State the blood parasite species.
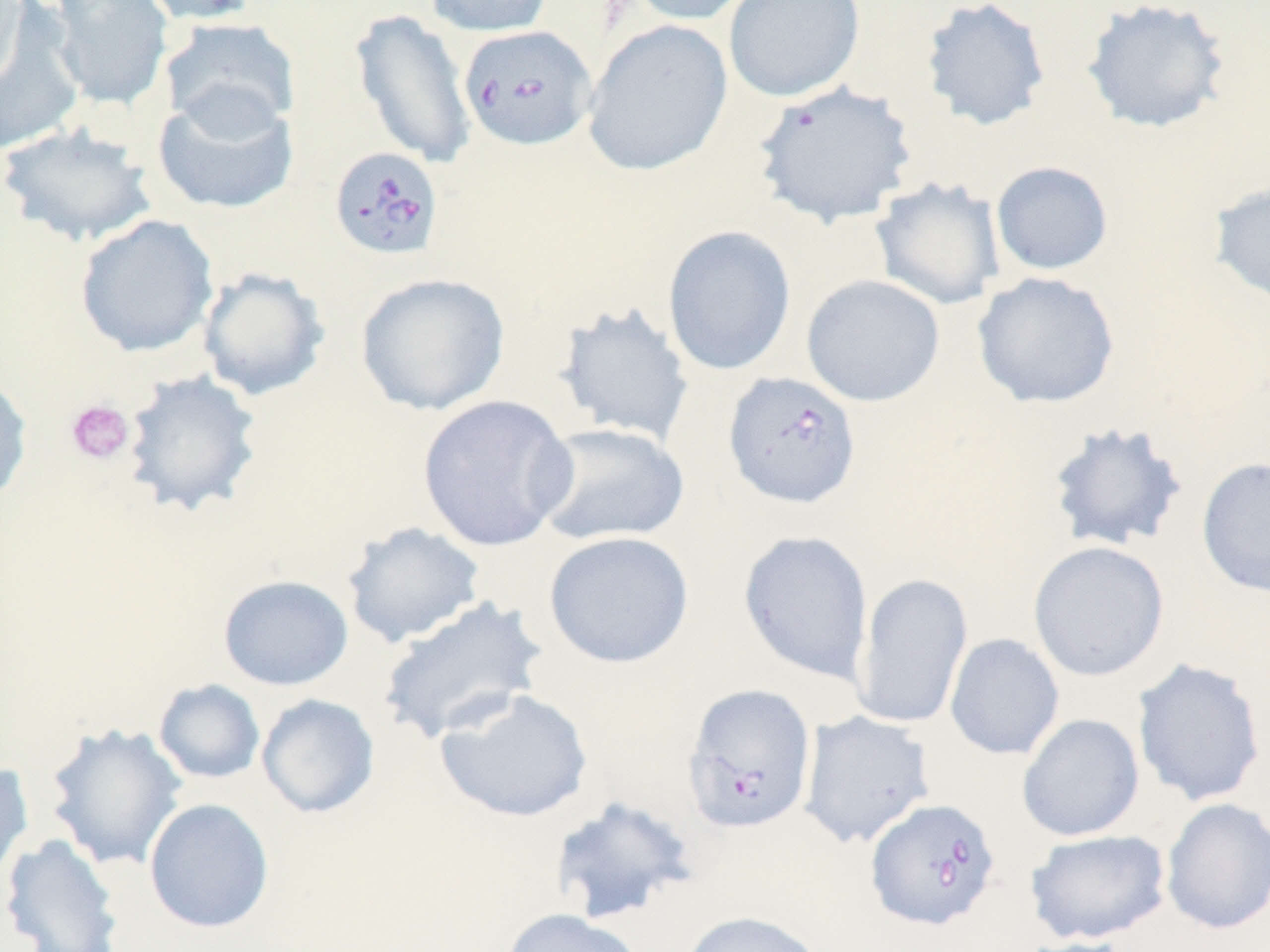

Babesia divergens.

Approximate bounding boxes as (x1, y1, x2, y2) in pixels. Babesia divergens-infected red blood cell locations: (458, 25, 597, 151), (328, 146, 445, 261), (722, 371, 862, 510), (682, 683, 817, 833), (865, 797, 1001, 931). Platelet locations: (65, 399, 135, 465). Uninfected red blood cell locations: (0, 0, 31, 99), (44, 0, 175, 112), (137, 0, 264, 25), (424, 0, 553, 37), (622, 0, 758, 26), (723, 0, 865, 103), (919, 0, 1051, 132), (1080, 0, 1232, 135), (349, 7, 477, 170), (0, 9, 85, 154), (159, 17, 301, 136), (581, 20, 733, 176), (752, 81, 919, 228), (151, 88, 298, 216), (0, 123, 159, 248), (991, 161, 1113, 275), (870, 177, 1005, 311), (1209, 179, 1270, 310), (74, 213, 219, 358), (662, 225, 797, 376), (197, 266, 330, 402), (355, 271, 510, 417), (972, 271, 1120, 409), (801, 274, 945, 407), (552, 301, 696, 447), (120, 369, 264, 519), (0, 372, 34, 507), (416, 394, 577, 552), (1045, 420, 1190, 554), (532, 422, 690, 547), (1196, 456, 1270, 598), (340, 521, 487, 649), (738, 530, 874, 684), (542, 531, 694, 669), (1027, 540, 1170, 682), (852, 571, 973, 730), (217, 574, 354, 691), (376, 597, 548, 746), (945, 633, 1065, 760), (1131, 657, 1267, 807), (153, 679, 265, 785), (434, 687, 594, 823), (256, 693, 380, 819), (798, 710, 936, 848), (1017, 713, 1145, 841), (42, 722, 188, 871), (0, 758, 34, 889), (547, 795, 701, 925), (1160, 797, 1270, 935), (144, 798, 275, 934), (1024, 828, 1172, 945), (0, 833, 125, 952), (501, 907, 643, 952), (678, 910, 825, 952), (1012, 937, 1139, 952). Thin blood smear. 1000x magnification. May-Grünwald-Giemsa-stained preparation. Optical microscopy. Single field of view. Image is 1270×952 pixels.